Outline each Plasmodium falciparum-infected red blood cell.
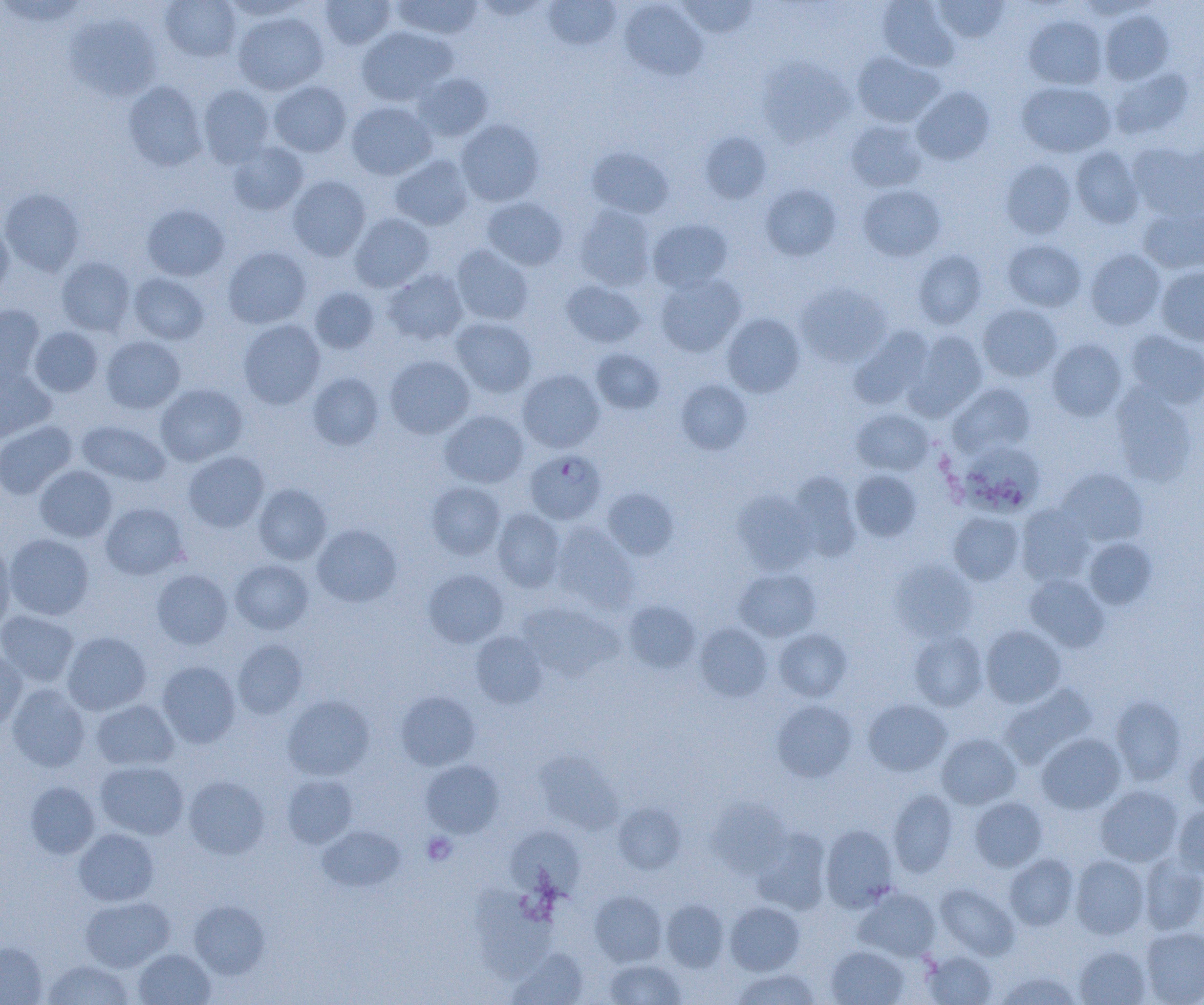
Approximate bounding boxes as named x1/y1/x2/y2 corners in pixels.
Plasmodium falciparum-infected red blood cells: (x1=525, y1=450, x2=606, y2=524).

Platelet locations: (x1=422, y1=832, x2=457, y2=865). Uninfected red blood cell locations: (x1=159, y1=0, x2=242, y2=62), (x1=220, y1=0, x2=311, y2=20), (x1=392, y1=0, x2=482, y2=40), (x1=542, y1=0, x2=621, y2=51), (x1=877, y1=0, x2=960, y2=72), (x1=319, y1=1, x2=395, y2=49), (x1=619, y1=1, x2=707, y2=80), (x1=677, y1=1, x2=758, y2=38), (x1=933, y1=1, x2=1009, y2=43), (x1=1099, y1=10, x2=1174, y2=85), (x1=233, y1=11, x2=328, y2=95), (x1=65, y1=12, x2=162, y2=102), (x1=1023, y1=15, x2=1107, y2=89), (x1=356, y1=26, x2=456, y2=105), (x1=852, y1=51, x2=943, y2=127), (x1=757, y1=57, x2=855, y2=146), (x1=1108, y1=67, x2=1194, y2=139), (x1=412, y1=72, x2=492, y2=141), (x1=123, y1=81, x2=207, y2=171), (x1=269, y1=81, x2=351, y2=157), (x1=1017, y1=81, x2=1115, y2=157), (x1=198, y1=85, x2=275, y2=168), (x1=912, y1=86, x2=995, y2=165), (x1=346, y1=101, x2=437, y2=180), (x1=456, y1=119, x2=544, y2=206), (x1=845, y1=119, x2=928, y2=193), (x1=699, y1=132, x2=772, y2=204), (x1=1128, y1=141, x2=1204, y2=221), (x1=228, y1=142, x2=309, y2=215), (x1=1070, y1=146, x2=1144, y2=228), (x1=587, y1=147, x2=674, y2=218), (x1=389, y1=154, x2=473, y2=230), (x1=1001, y1=158, x2=1076, y2=239), (x1=287, y1=175, x2=370, y2=261), (x1=761, y1=185, x2=841, y2=260), (x1=858, y1=185, x2=946, y2=261), (x1=1, y1=188, x2=85, y2=277), (x1=482, y1=197, x2=568, y2=270), (x1=142, y1=204, x2=229, y2=281), (x1=574, y1=205, x2=656, y2=290), (x1=1139, y1=206, x2=1204, y2=274), (x1=349, y1=212, x2=435, y2=292), (x1=648, y1=219, x2=733, y2=293), (x1=0, y1=221, x2=14, y2=300), (x1=1003, y1=239, x2=1086, y2=312), (x1=451, y1=244, x2=533, y2=326), (x1=223, y1=246, x2=311, y2=328), (x1=1085, y1=249, x2=1165, y2=330), (x1=912, y1=250, x2=988, y2=329), (x1=56, y1=256, x2=135, y2=335), (x1=1156, y1=267, x2=1204, y2=346), (x1=383, y1=269, x2=469, y2=345), (x1=128, y1=272, x2=209, y2=344), (x1=655, y1=273, x2=746, y2=356), (x1=561, y1=280, x2=646, y2=348), (x1=795, y1=283, x2=890, y2=367), (x1=308, y1=287, x2=380, y2=354), (x1=978, y1=303, x2=1062, y2=382), (x1=0, y1=305, x2=45, y2=385), (x1=722, y1=313, x2=805, y2=397), (x1=450, y1=317, x2=537, y2=397), (x1=238, y1=319, x2=325, y2=409), (x1=850, y1=326, x2=935, y2=409), (x1=29, y1=327, x2=104, y2=397), (x1=905, y1=330, x2=988, y2=418), (x1=1124, y1=330, x2=1204, y2=409), (x1=101, y1=336, x2=185, y2=414), (x1=1047, y1=338, x2=1127, y2=421), (x1=590, y1=348, x2=665, y2=415), (x1=385, y1=355, x2=475, y2=439), (x1=0, y1=367, x2=55, y2=442), (x1=517, y1=368, x2=604, y2=453), (x1=308, y1=373, x2=383, y2=450), (x1=676, y1=379, x2=752, y2=454), (x1=949, y1=383, x2=1036, y2=457), (x1=155, y1=384, x2=247, y2=466), (x1=1111, y1=386, x2=1197, y2=486), (x1=852, y1=408, x2=933, y2=475), (x1=440, y1=410, x2=529, y2=488), (x1=77, y1=420, x2=171, y2=487), (x1=0, y1=421, x2=77, y2=499), (x1=959, y1=441, x2=1045, y2=515), (x1=183, y1=451, x2=269, y2=533), (x1=35, y1=465, x2=117, y2=542), (x1=1057, y1=468, x2=1148, y2=546), (x1=850, y1=470, x2=921, y2=542), (x1=789, y1=472, x2=861, y2=561), (x1=426, y1=482, x2=505, y2=559), (x1=253, y1=484, x2=331, y2=564), (x1=601, y1=488, x2=678, y2=560), (x1=732, y1=491, x2=815, y2=574), (x1=100, y1=503, x2=188, y2=579), (x1=1016, y1=504, x2=1095, y2=587), (x1=492, y1=509, x2=565, y2=591), (x1=948, y1=512, x2=1024, y2=585), (x1=552, y1=523, x2=638, y2=612), (x1=312, y1=524, x2=401, y2=607), (x1=5, y1=533, x2=94, y2=620), (x1=1084, y1=538, x2=1157, y2=609), (x1=0, y1=541, x2=16, y2=630), (x1=230, y1=559, x2=313, y2=634), (x1=890, y1=560, x2=976, y2=641), (x1=734, y1=567, x2=821, y2=641), (x1=152, y1=569, x2=233, y2=649), (x1=424, y1=570, x2=509, y2=647), (x1=1025, y1=575, x2=1110, y2=652), (x1=623, y1=600, x2=700, y2=673), (x1=518, y1=601, x2=620, y2=680), (x1=0, y1=610, x2=79, y2=687), (x1=693, y1=623, x2=772, y2=701), (x1=980, y1=626, x2=1066, y2=708), (x1=774, y1=628, x2=851, y2=701), (x1=62, y1=631, x2=152, y2=715), (x1=470, y1=631, x2=547, y2=708), (x1=909, y1=631, x2=987, y2=711), (x1=232, y1=639, x2=307, y2=719), (x1=0, y1=648, x2=27, y2=732), (x1=157, y1=661, x2=240, y2=748), (x1=999, y1=683, x2=1097, y2=769), (x1=6, y1=684, x2=90, y2=772), (x1=396, y1=691, x2=480, y2=770), (x1=282, y1=695, x2=374, y2=780), (x1=1110, y1=696, x2=1186, y2=785), (x1=91, y1=699, x2=178, y2=770), (x1=863, y1=699, x2=951, y2=776), (x1=772, y1=700, x2=857, y2=781), (x1=1036, y1=733, x2=1126, y2=814), (x1=937, y1=734, x2=1021, y2=809), (x1=1184, y1=745, x2=1204, y2=812), (x1=421, y1=760, x2=504, y2=838), (x1=95, y1=761, x2=188, y2=839), (x1=282, y1=774, x2=357, y2=848), (x1=184, y1=776, x2=269, y2=859), (x1=24, y1=781, x2=100, y2=859), (x1=1095, y1=785, x2=1183, y2=866), (x1=888, y1=789, x2=957, y2=877), (x1=969, y1=797, x2=1047, y2=871), (x1=708, y1=799, x2=790, y2=877), (x1=612, y1=802, x2=686, y2=874), (x1=1172, y1=804, x2=1204, y2=878), (x1=317, y1=825, x2=405, y2=892), (x1=821, y1=825, x2=899, y2=911), (x1=74, y1=828, x2=159, y2=906), (x1=507, y1=828, x2=584, y2=900), (x1=752, y1=829, x2=831, y2=914), (x1=1004, y1=854, x2=1079, y2=930), (x1=1140, y1=854, x2=1204, y2=935), (x1=1070, y1=855, x2=1149, y2=939), (x1=936, y1=884, x2=1018, y2=959), (x1=855, y1=888, x2=940, y2=961), (x1=471, y1=890, x2=557, y2=981), (x1=590, y1=890, x2=666, y2=967), (x1=80, y1=896, x2=174, y2=971), (x1=661, y1=899, x2=728, y2=971), (x1=189, y1=900, x2=270, y2=979), (x1=724, y1=901, x2=805, y2=975), (x1=1141, y1=926, x2=1204, y2=1004), (x1=0, y1=942, x2=47, y2=1005), (x1=1075, y1=945, x2=1151, y2=1005), (x1=826, y1=946, x2=909, y2=1004), (x1=507, y1=948, x2=588, y2=1005), (x1=134, y1=949, x2=215, y2=1005), (x1=924, y1=951, x2=996, y2=1004), (x1=604, y1=958, x2=687, y2=1004), (x1=43, y1=959, x2=134, y2=1005), (x1=731, y1=968, x2=821, y2=1004), (x1=996, y1=971, x2=1080, y2=1004). Slide-level diagnosis: Plasmodium falciparum. Captured at 1000x magnification. Image is 1204×1005 pixels. Optical microscopy. One field of a larger specimen. Thin blood smear.